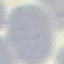 Malaria status: uninfected. Giemsa stain. Cell patch, automatically extracted from a larger field of view and resized to 64 × 64 pixels. Acquired by smartphone through the microscope eyepiece. Thin blood smear.